Point out each Plasmodium parasite and classify it by life-cycle stage.
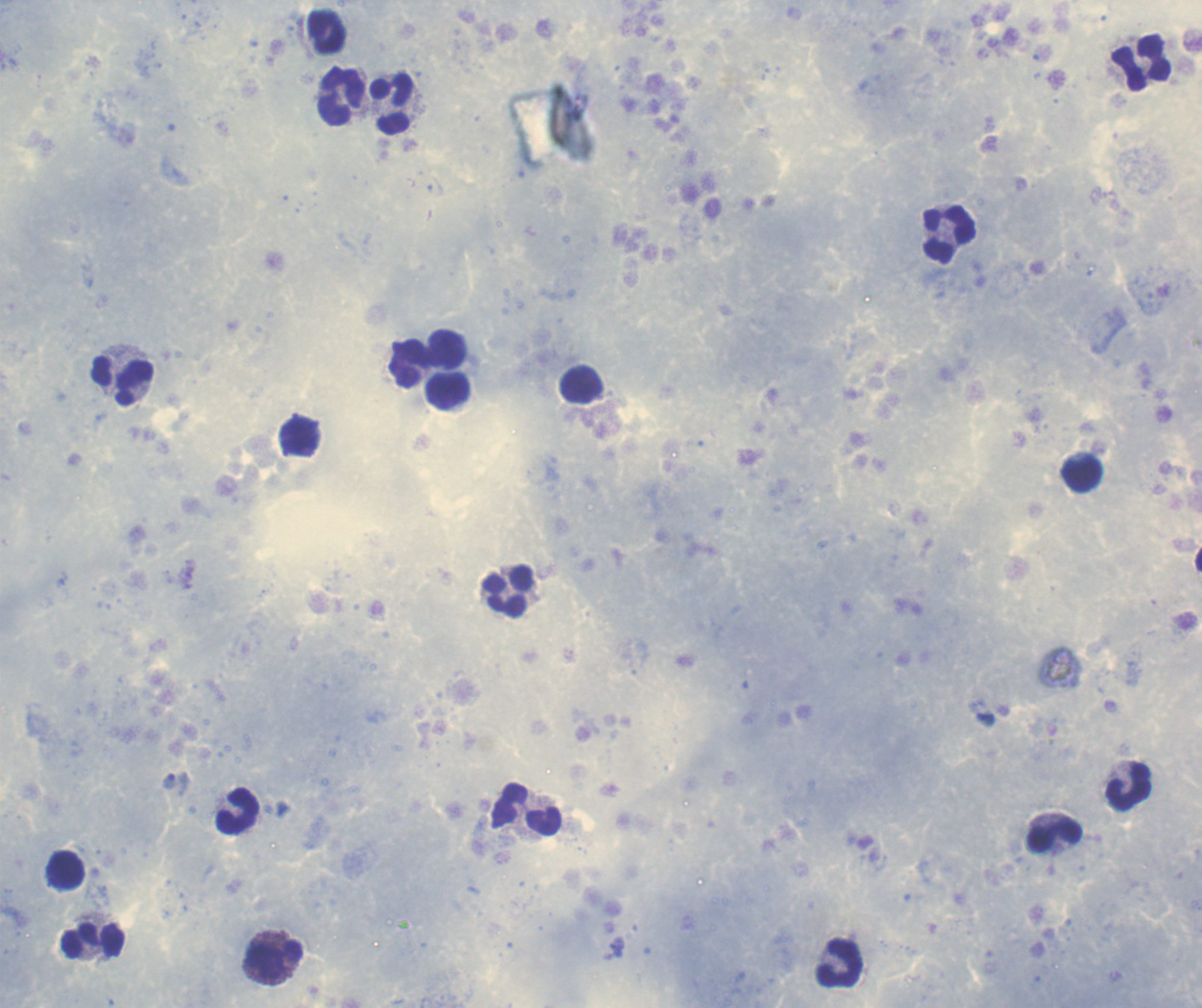
Approximate centers as {x, y} in pixels.
Trophozoites: {986, 719}, {170, 781}.
No schizont or gametocyte forms observed.

Approximate centers as {x, y} in pixels. Leukocyte locations: {327, 33}, {1141, 62}, {341, 97}, {392, 105}, {949, 235}, {447, 349}, {410, 364}, {123, 381}, {583, 385}, {447, 392}, {1081, 474}, {508, 592}, {1129, 787}, {526, 809}, {238, 810}, {1054, 838}, {94, 941}, {274, 960}, {841, 963}. Coloration quality: good. Single field of view. Romanowsky-stained preparation. Background quality: satisfactory. Image is 1202×1008 pixels. Previously used in an actual diagnosis. Thick blood film. 100x magnification.